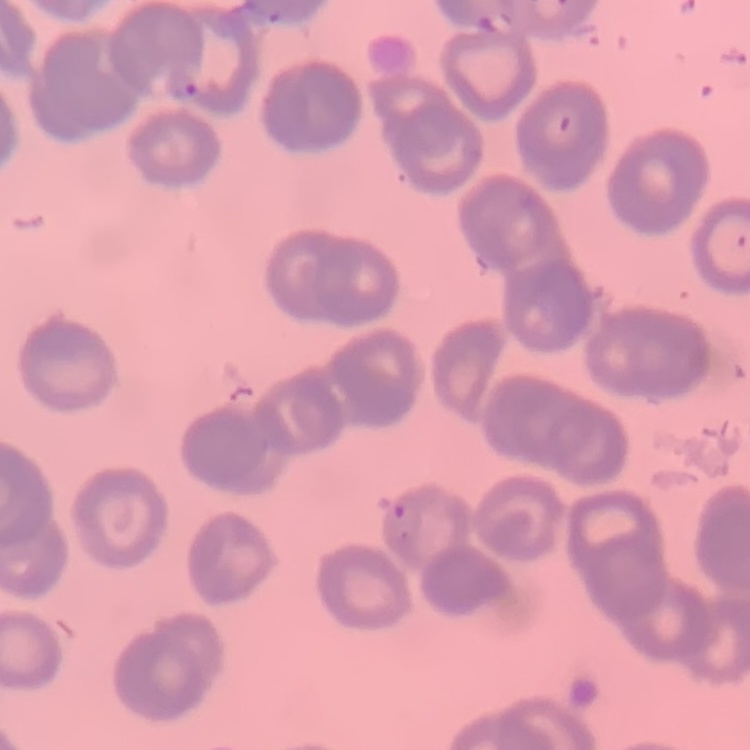 The red blood cells exhibit rouleaux formation. One tile cut from a larger photomicrograph. Thin blood smear. Stained with either Field's or Giemsa.